Report the malaria status of this cell.
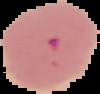
Parasitized.

The area outside the segmented cell region is set to black. From a thin blood film. Image is 100×94 pixels.